Locate every blood parasite and identify its species.
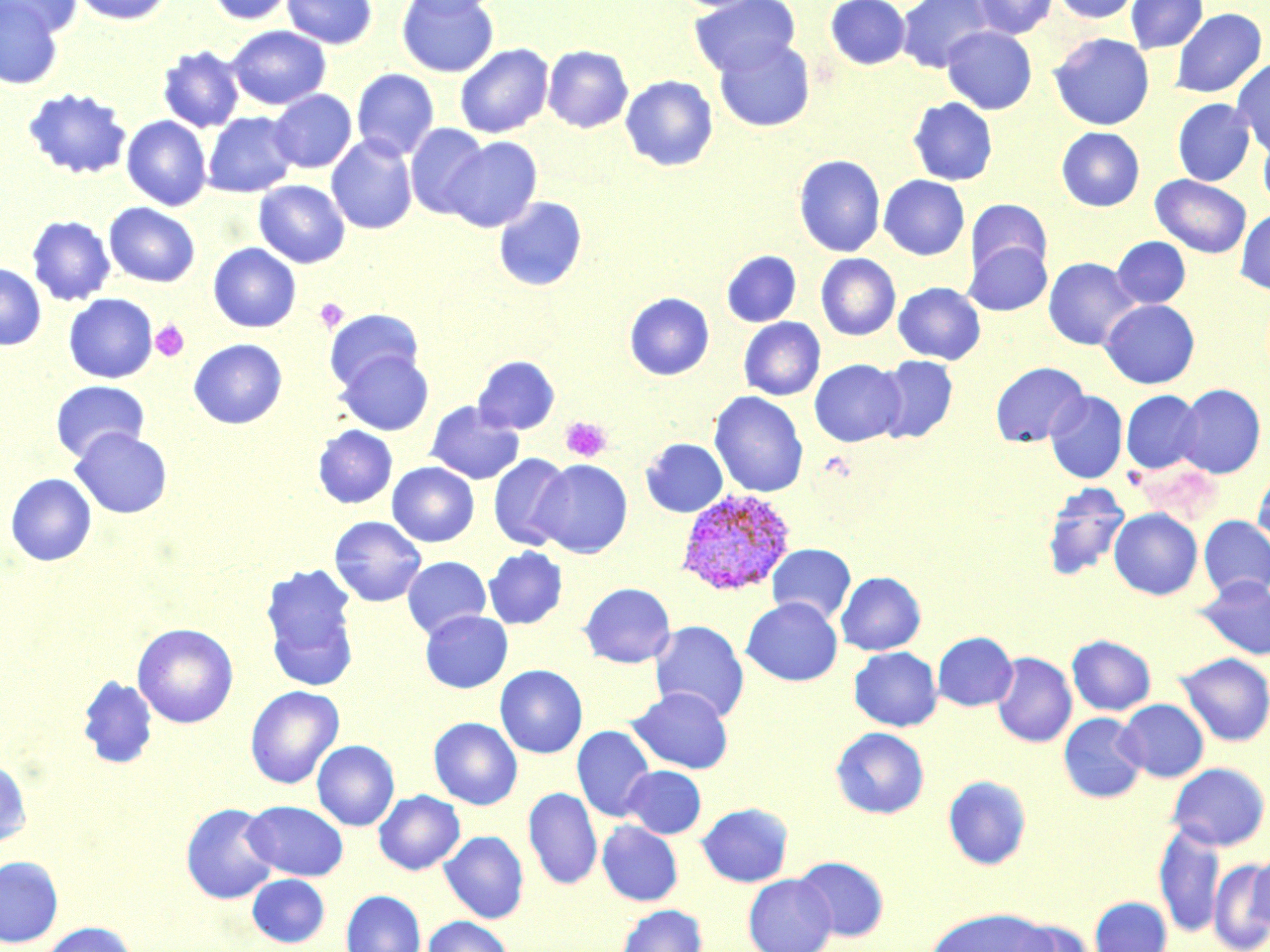
Approximate bounding boxes as [x1, y1, x2, y2] in pixels.
Plasmodium vivax-infected red blood cells: [679, 490, 800, 597].
No Plasmodium falciparum, Plasmodium ovale, Plasmodium malariae, Babesia divergens, or Trypanosoma brucei observed.

Summary:
  - Platelet locations: [315, 298, 348, 333], [151, 320, 189, 362], [560, 416, 612, 462]
  - Uninfected red blood cell locations: [0, 0, 82, 37], [72, 0, 174, 25], [205, 0, 296, 25], [282, 0, 377, 49], [396, 0, 500, 77], [401, 0, 500, 18], [690, 0, 801, 78], [825, 0, 911, 69], [896, 0, 996, 73], [973, 0, 1057, 38], [1051, 0, 1141, 23], [1126, 0, 1206, 53], [0, 1, 64, 88], [1170, 7, 1267, 98], [226, 25, 331, 109], [941, 26, 1037, 114], [1049, 33, 1154, 130], [714, 37, 815, 132], [455, 44, 554, 138], [157, 45, 245, 133], [543, 45, 633, 133], [1232, 58, 1270, 157], [351, 68, 440, 160], [620, 75, 718, 171], [1209, 78, 1268, 181], [23, 87, 132, 180], [268, 89, 356, 173], [908, 97, 998, 186], [1173, 98, 1255, 186], [203, 112, 297, 197], [122, 115, 211, 210], [405, 123, 491, 220], [1057, 127, 1145, 211], [1258, 128, 1270, 212], [326, 135, 418, 235], [443, 136, 542, 232], [794, 154, 885, 257], [1151, 174, 1251, 258], [879, 175, 969, 260], [253, 180, 350, 268], [493, 196, 587, 291], [966, 198, 1052, 278], [104, 202, 200, 287], [1235, 209, 1270, 295], [27, 216, 115, 306], [1112, 236, 1190, 308], [963, 240, 1052, 316], [208, 243, 301, 332], [721, 250, 801, 327], [816, 253, 900, 340], [1043, 257, 1141, 350], [0, 263, 46, 350], [893, 282, 986, 364], [624, 292, 714, 380], [64, 293, 157, 383], [1100, 299, 1200, 389], [325, 309, 423, 393], [739, 317, 825, 400], [188, 338, 287, 429], [335, 349, 434, 435], [473, 355, 560, 434], [875, 355, 958, 443], [809, 359, 906, 447], [990, 361, 1089, 447], [50, 380, 150, 463], [1175, 384, 1266, 478], [1045, 390, 1128, 483], [1121, 390, 1204, 474], [709, 391, 808, 497], [425, 401, 524, 484], [312, 425, 397, 509], [70, 427, 172, 518], [641, 438, 728, 517], [488, 453, 573, 551], [534, 459, 632, 558], [387, 462, 479, 547], [1253, 469, 1270, 555], [5, 473, 97, 566], [1041, 483, 1130, 582], [1109, 508, 1203, 599], [1199, 515, 1270, 599], [329, 516, 426, 606], [767, 544, 856, 623], [483, 546, 568, 629], [402, 556, 491, 639], [260, 562, 360, 691], [836, 571, 926, 655], [1193, 575, 1270, 660], [579, 582, 675, 668], [741, 598, 843, 686], [420, 610, 512, 693], [650, 620, 749, 722], [132, 623, 238, 728], [933, 632, 1018, 711], [1067, 635, 1156, 715], [848, 647, 942, 731], [992, 652, 1077, 747], [1176, 652, 1270, 747], [495, 665, 587, 758], [78, 675, 158, 769], [245, 685, 344, 789], [628, 687, 733, 774], [1116, 699, 1209, 782], [1058, 713, 1147, 803], [428, 717, 523, 809], [572, 726, 656, 822], [831, 727, 929, 818], [312, 740, 399, 831], [0, 759, 32, 847], [1166, 762, 1269, 851], [622, 765, 706, 838], [943, 775, 1032, 870], [524, 787, 603, 890], [374, 790, 465, 874], [243, 801, 347, 880], [181, 802, 279, 904], [697, 802, 793, 887], [597, 820, 683, 906], [1153, 823, 1224, 937], [439, 830, 528, 924], [1249, 850, 1270, 936], [0, 855, 63, 948], [794, 856, 889, 941], [1209, 859, 1270, 950], [247, 873, 330, 948], [743, 874, 837, 952], [341, 889, 425, 952], [1089, 896, 1172, 952], [615, 904, 708, 952], [925, 907, 1055, 952], [423, 916, 512, 952], [1009, 918, 1089, 952], [38, 922, 137, 952]
  - Slide-level diagnosis: Plasmodium vivax
  - Image size: 1270×952 pixels
  - Preparation: thin blood film
  - Magnification: 1000x
  - Stain: May-Grünwald-Giemsa
  - Modality: optical microscopy
  - Field of view: one of a larger specimen